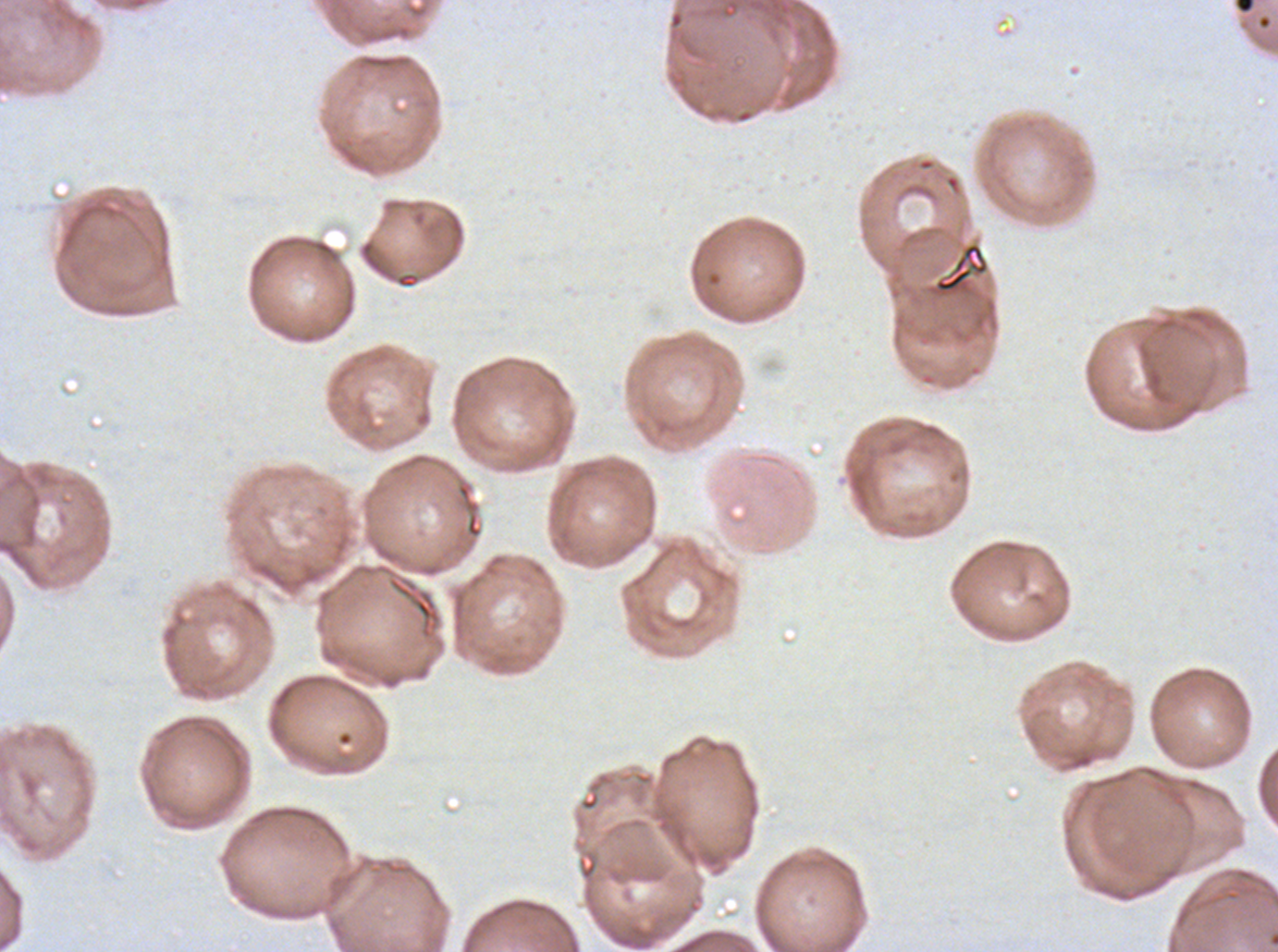 Approximate bounding boxes as [x1, y1, x2, y2] in pixels. Debris locations: [933, 241, 989, 294]. Image is 1278×952 pixels. Giemsa-stained preparation. P. falciparum cultured ex vivo for 24 to 48 hours, from a patient in The Gambia. One sub-image of a larger composite. Thin blood smear.